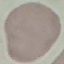
result = negative for malaria parasites
capture = smartphone through the microscope eyepiece
stain = Giemsa
image type = cell patch, automatically extracted from a larger field of view and resized to 64 × 64 pixels
preparation = thin smear